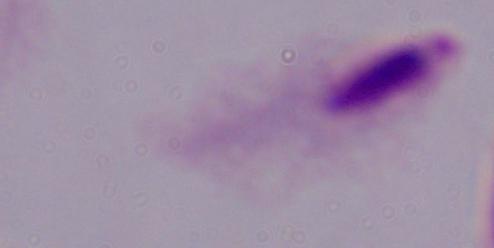
identification = trichomonad
modality = micrograph
magnification = 1000x